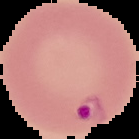

image type = segmented cell region with the area outside set to black
malaria status = parasitized
image size = 139×139 pixels
preparation = thin blood film